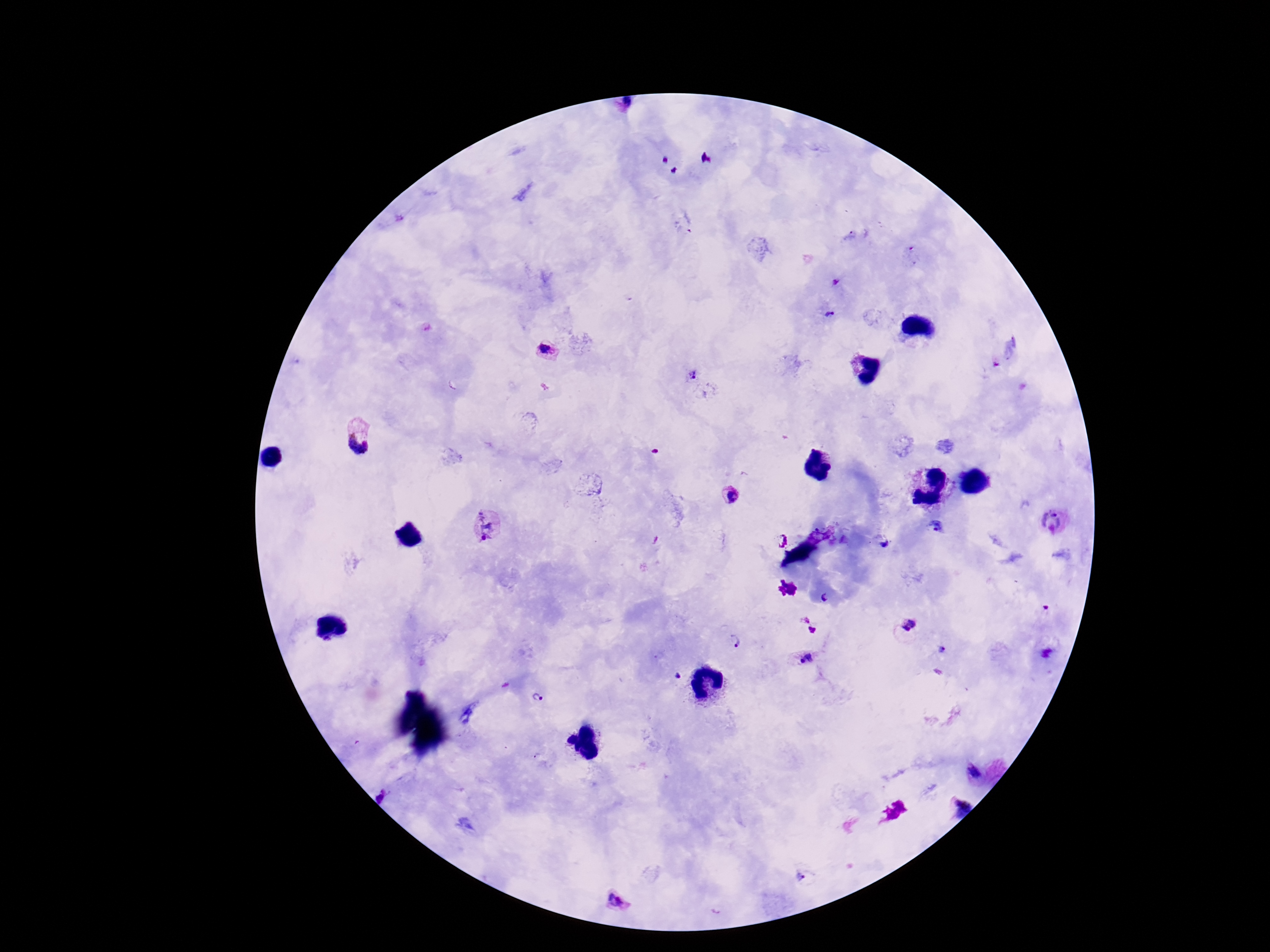

field_of_view: one from this slide
plasmodium_parasite_locations: 'approximate centers as {x, y} in pixels: {849, 237}, {834, 281}, {829, 313}, {545, 348}, {691, 374}, {359, 434}, {729, 497}, {1054, 521}, {483, 525}, {934, 528}, {781, 539}, {884, 544}, {827, 598}, {907, 623}, {811, 625}, {733, 641}, {805, 658}, {676, 675}, {540, 698}, {975, 772}, {957, 803}, {803, 876}, {616, 902}'
image_size: 1270×952 pixels
capture: smartphone camera through the microscope eyepiece
patient_malaria_status: positive
magnification: 100x
preparation: thick blood film
stain: Giemsa